Assess the morphology of the erythrocytes.
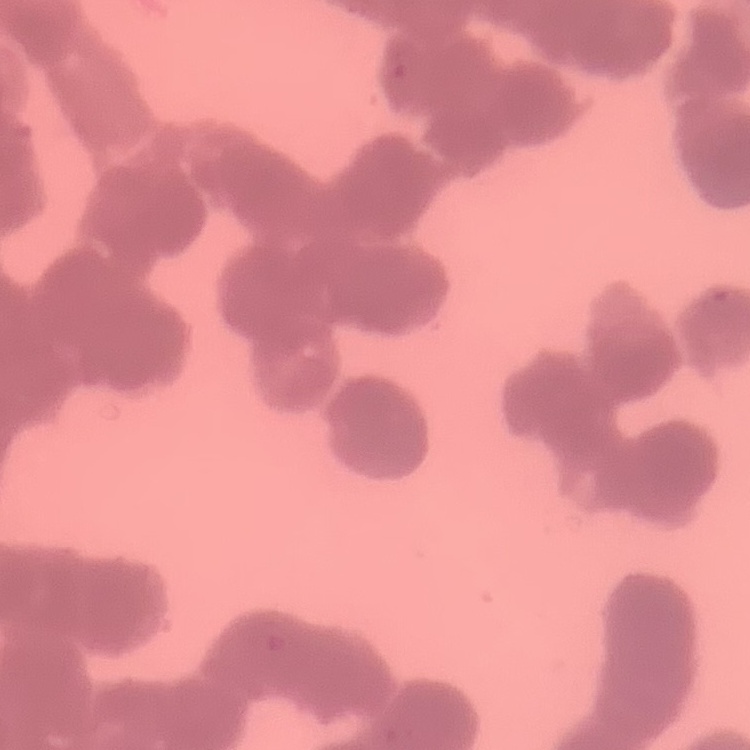
Rouleaux formation.

Summary:
  - Image type: square crop of a larger photomicrograph
  - Stain: Field's or Giemsa
  - Preparation: thin peripheral smear